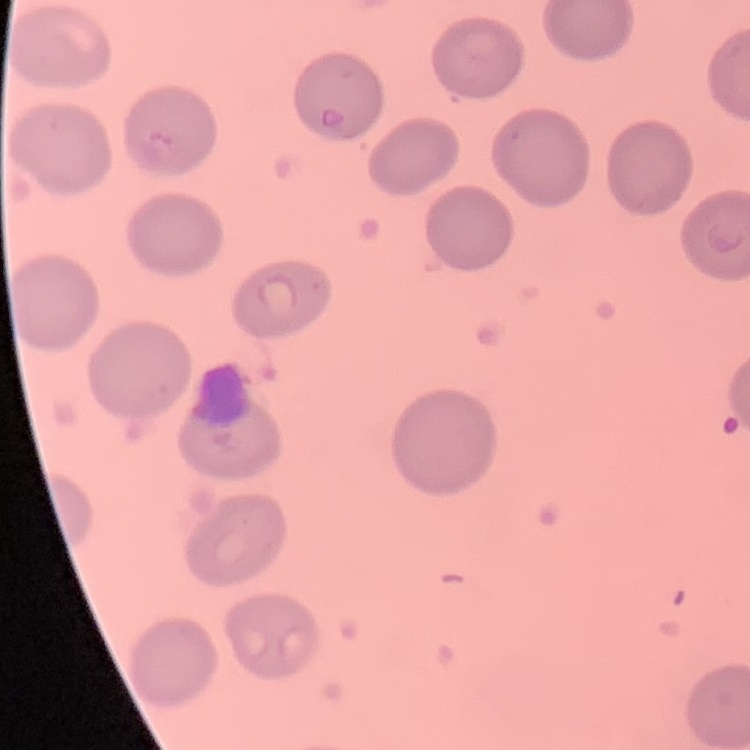
red blood cell morphology = no rouleaux formation
image type = one tile cut from a larger photomicrograph
stain = Field's or Giemsa
preparation = thin blood film